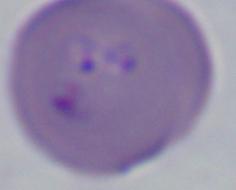

Summary:
  - Modality: micrograph
  - Identification: Babesia
  - Magnification: 1000x